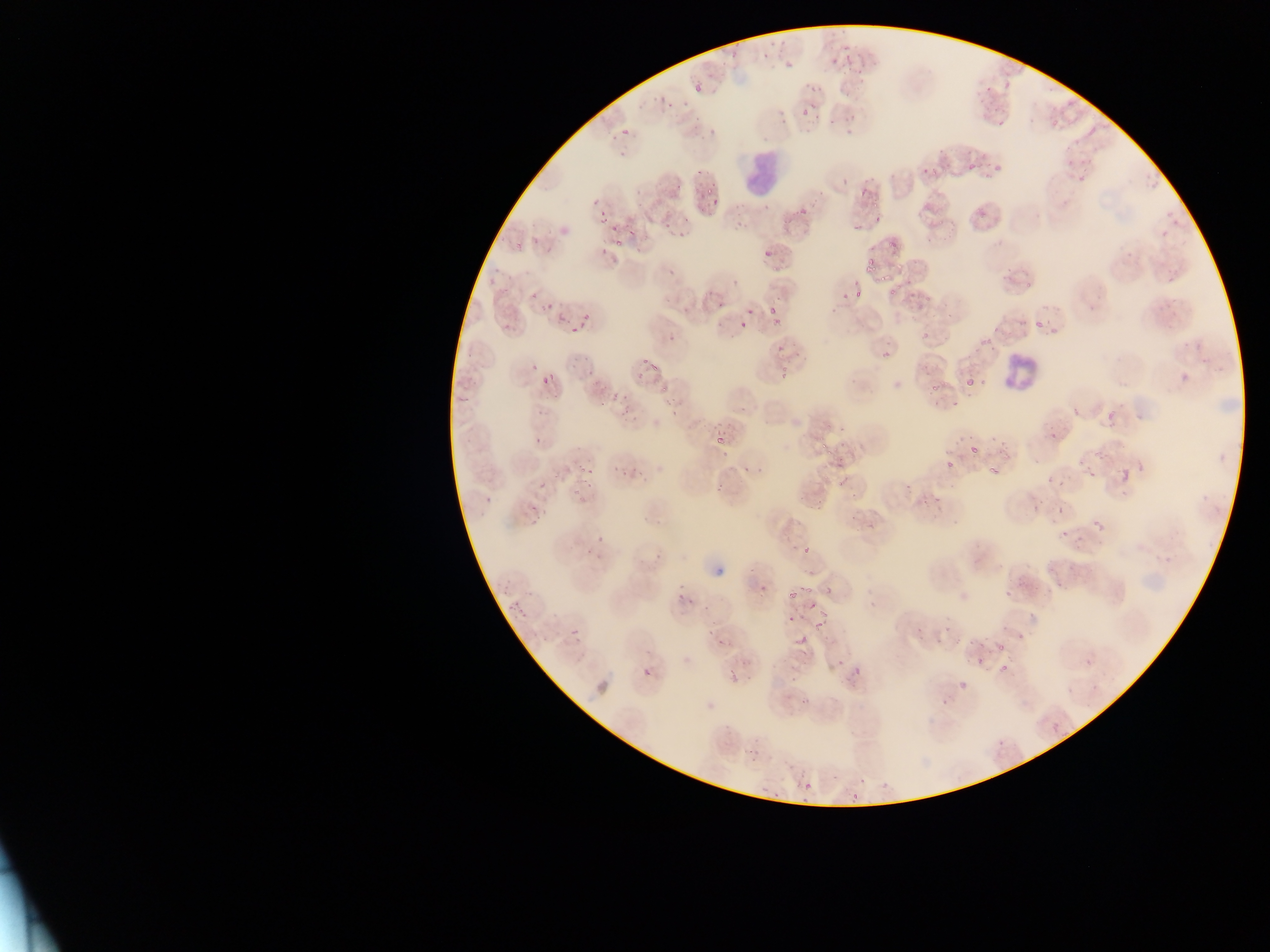

Approximate bounding boxes as (left, top, right, bottom) in pixels. Plasmodium parasite locations: (759, 40, 781, 61), (832, 42, 850, 62), (778, 52, 792, 68), (846, 65, 865, 76), (692, 81, 702, 92), (806, 82, 818, 95), (982, 84, 991, 92), (660, 92, 673, 110), (682, 97, 696, 106), (799, 97, 814, 122), (770, 104, 788, 121), (692, 111, 706, 125), (1045, 111, 1064, 135), (827, 118, 834, 127), (843, 124, 856, 135), (623, 128, 634, 135), (1088, 128, 1095, 136), (611, 129, 623, 143), (697, 134, 709, 144), (937, 139, 947, 151), (619, 150, 629, 161), (975, 150, 987, 161), (1059, 153, 1073, 165), (1068, 154, 1093, 161), (992, 158, 1003, 171), (969, 164, 977, 173), (920, 168, 926, 179), (927, 168, 943, 175), (1146, 168, 1165, 187), (838, 171, 851, 185), (1078, 172, 1086, 185), (856, 183, 867, 203), (704, 185, 716, 198), (589, 194, 605, 208), (599, 197, 616, 223), (708, 197, 720, 205), (792, 201, 810, 217), (974, 203, 987, 217), (1164, 211, 1183, 229), (872, 215, 882, 228), (849, 219, 860, 235), (609, 220, 625, 231), (1159, 225, 1168, 237), (623, 227, 636, 239), (512, 235, 537, 251), (615, 238, 622, 247), (760, 241, 779, 262), (884, 242, 899, 251), (864, 257, 877, 275), (1003, 266, 1016, 284), (877, 275, 892, 287), (911, 277, 929, 300), (1024, 278, 1037, 296), (494, 284, 513, 298), (845, 287, 852, 296), (853, 288, 864, 299), (884, 288, 899, 297), (528, 290, 542, 305), (827, 300, 838, 316), (540, 302, 554, 317), (746, 304, 757, 317), (767, 305, 777, 317), (578, 312, 589, 331), (733, 314, 747, 331), (506, 315, 520, 332), (767, 318, 780, 333), (1030, 319, 1043, 333), (1050, 324, 1060, 334), (565, 327, 576, 336), (919, 328, 928, 338), (976, 336, 990, 349), (777, 338, 787, 353), (879, 344, 892, 359), (637, 357, 650, 370), (650, 358, 659, 375), (530, 361, 542, 370), (777, 362, 795, 384), (1175, 367, 1198, 385), (977, 372, 989, 389), (546, 374, 555, 382), (539, 376, 549, 387), (965, 377, 974, 385), (930, 383, 940, 392), (657, 384, 670, 392), (610, 392, 621, 401), (952, 392, 970, 410), (664, 396, 681, 403), (1107, 400, 1126, 424), (1060, 401, 1091, 421), (595, 402, 604, 408), (616, 402, 631, 416), (929, 404, 939, 411), (668, 408, 679, 416), (630, 414, 639, 418), (822, 419, 830, 428), (838, 420, 849, 436), (1043, 426, 1060, 447), (952, 432, 966, 442), (988, 432, 1007, 455), (536, 433, 548, 444), (710, 433, 727, 447), (838, 434, 847, 450), (820, 442, 834, 455), (968, 442, 981, 457), (1095, 452, 1112, 465), (945, 457, 954, 469), (612, 460, 625, 473), (986, 464, 1000, 477), (757, 465, 762, 473), (575, 466, 587, 475), (617, 466, 629, 474), (1119, 468, 1130, 483), (586, 469, 591, 486), (1058, 471, 1073, 485), (1090, 473, 1102, 487), (1047, 475, 1055, 483), (539, 480, 548, 491), (837, 480, 847, 489), (575, 483, 584, 492), (904, 484, 912, 492), (811, 490, 831, 512), (486, 491, 499, 503), (921, 491, 934, 507), (848, 494, 860, 501), (933, 494, 949, 510), (1034, 500, 1044, 508), (843, 513, 861, 529), (529, 514, 545, 523), (1092, 518, 1107, 533), (1059, 526, 1072, 539), (584, 536, 598, 554), (1075, 536, 1088, 550), (802, 546, 810, 555), (1053, 576, 1066, 590), (796, 580, 819, 596), (1004, 584, 1012, 597), (786, 585, 805, 603), (757, 586, 766, 600), (506, 595, 521, 607), (679, 595, 689, 607), (515, 600, 527, 620), (696, 600, 711, 610), (806, 601, 814, 610), (813, 607, 831, 635), (1026, 608, 1042, 617), (782, 615, 798, 625), (917, 624, 923, 636), (571, 627, 581, 638), (704, 627, 716, 638), (1017, 628, 1034, 638), (935, 629, 946, 645), (792, 631, 807, 647), (718, 635, 735, 646), (963, 635, 981, 649), (995, 643, 1005, 652), (976, 653, 991, 672), (1084, 657, 1094, 668), (789, 659, 810, 689), (999, 660, 1009, 675), (849, 661, 867, 675), (727, 664, 738, 684), (640, 666, 659, 677), (957, 680, 967, 689), (1087, 680, 1100, 692), (1065, 688, 1072, 696), (941, 696, 956, 705), (798, 697, 809, 710), (1051, 724, 1060, 733), (996, 735, 1012, 751), (749, 751, 760, 770), (855, 772, 863, 784), (791, 775, 801, 789), (880, 777, 890, 791), (758, 781, 767, 792), (803, 781, 811, 790), (769, 789, 778, 797), (852, 793, 860, 802), (798, 800, 815, 806) | approximate (x, y) pixel centers of objects too small to bound: (698, 171), (744, 473), (1059, 511). Leukocyte locations: (738, 155, 779, 195), (994, 348, 1034, 392). Image is 1270×952 pixels. Collected in Ghana. Single field of view. Thin blood film. Photographed through a microscope with a mobile-phone camera.